Assess this cell for malaria.
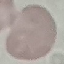

Uninfected.

Cell patch, automatically extracted from a larger field of view and resized to 64 × 64 pixels. Thin blood film. Giemsa stain. Photographed with a smartphone camera at the microscope eyepiece.